Give the extent of all Plasmodium parasites.
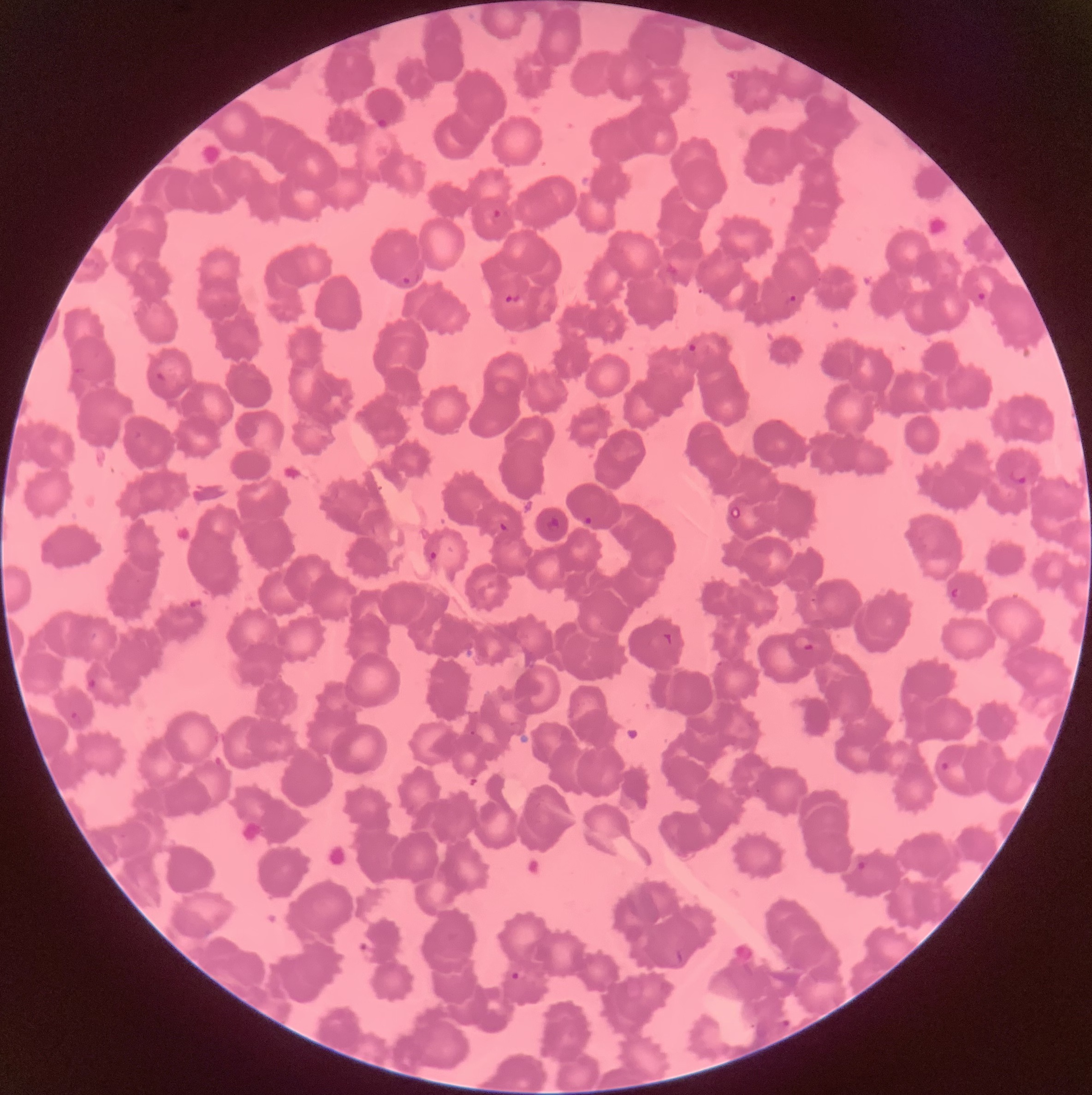
Approximate bounding boxes as (x1,y1)-(x2,y2) corner pairs in pixels.
Plasmodium parasites: (376,116)-(390,131), (491,209)-(505,222), (400,272)-(420,286), (976,291)-(988,302), (503,292)-(523,305), (784,292)-(799,312), (686,339)-(710,358), (154,371)-(168,383), (1009,466)-(1028,485), (581,514)-(593,529), (543,516)-(562,534), (497,521)-(510,533), (427,549)-(439,563), (949,586)-(965,607), (661,631)-(675,647), (793,636)-(814,654), (85,675)-(100,694), (69,710)-(83,732), (469,729)-(477,736), (937,760)-(952,774), (855,860)-(869,873), (356,941)-(377,962), (674,949)-(684,965), (509,971)-(522,982), (773,1020)-(790,1036).

modality = optical microscopy
image size = 1092×1095 pixels
preparation = thin blood smear
red blood cell morphology = rouleaux formation